Assess for parasitized red blood cells.
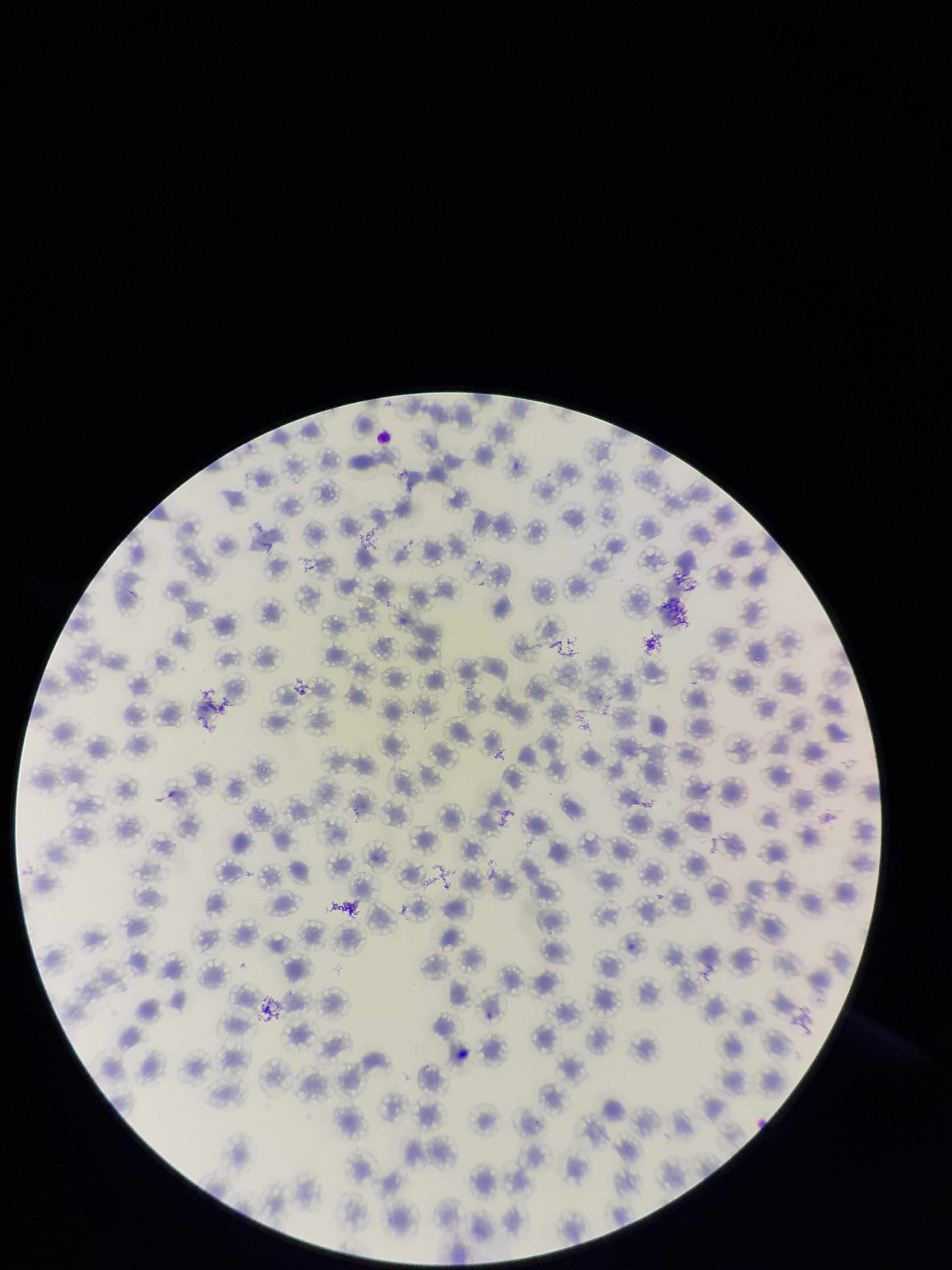
None detected.

stain = Giemsa
red blood cell count = 130
parasitized red blood cell count = 0
capture = smartphone photograph through the microscope eyepiece
species reported for this patient = Plasmodium falciparum
preparation = thin
image size = 952×1270 pixels
patient malaria status = infected
field of view = single